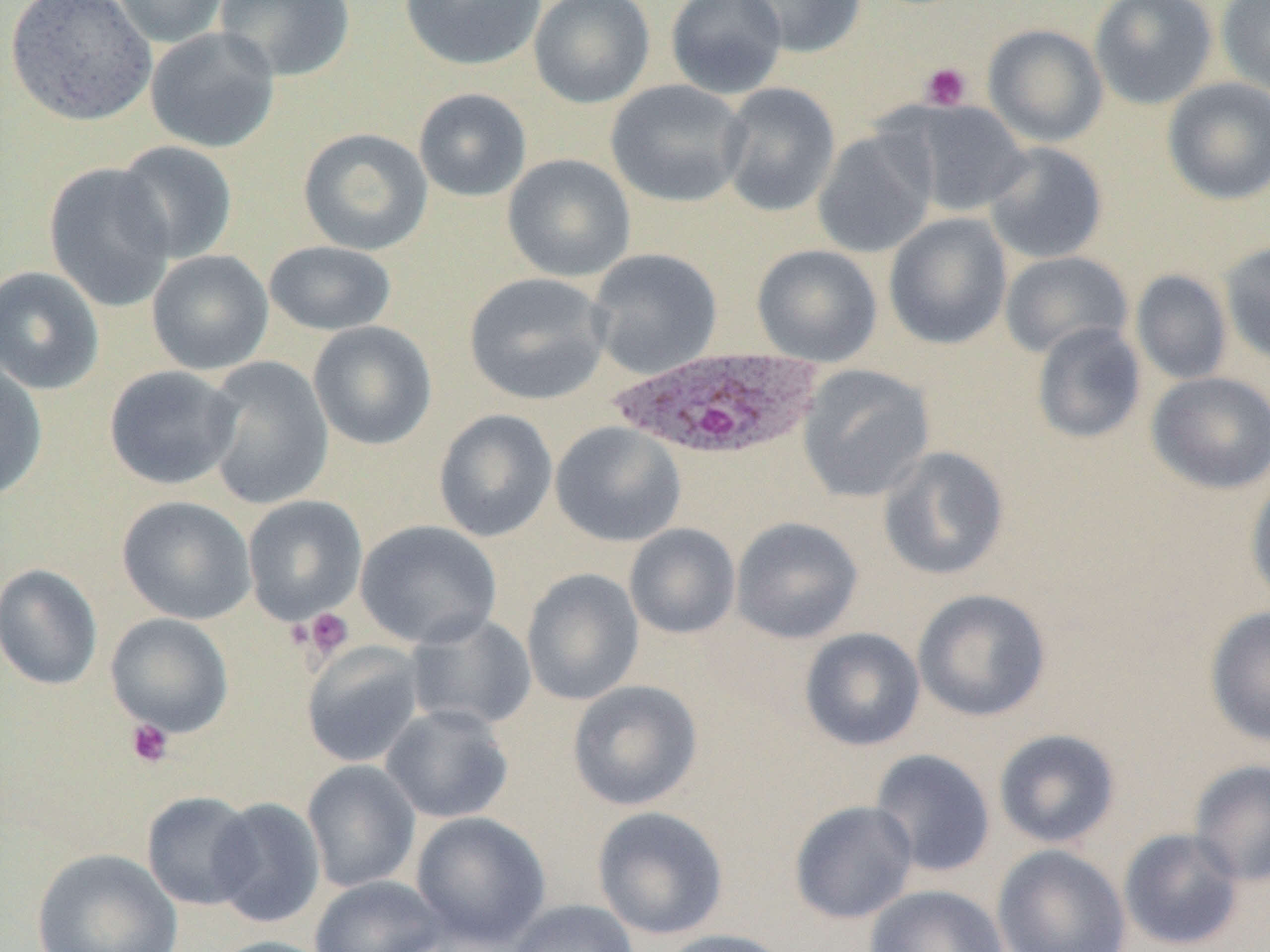
{
  "slide_level_diagnosis": "Plasmodium ovale",
  "uninfected_red_blood_cell_locations": "approximate bounding boxes as (x1, y1, x2, y2) in pixels: (3, 0, 157, 126), (109, 0, 230, 48), (213, 0, 355, 82), (399, 0, 547, 71), (529, 0, 655, 108), (665, 0, 788, 99), (733, 0, 867, 58), (1089, 0, 1218, 109), (1216, 0, 1270, 97), (983, 23, 1108, 147), (145, 26, 280, 153), (1162, 77, 1270, 205), (605, 79, 750, 208), (718, 82, 840, 217), (413, 88, 532, 202), (902, 101, 1032, 216), (298, 127, 433, 255), (813, 128, 937, 258), (113, 141, 238, 264), (983, 142, 1108, 264), (502, 153, 636, 282), (44, 162, 176, 312), (883, 213, 1013, 350), (1219, 240, 1270, 365), (264, 241, 397, 336), (751, 244, 883, 366), (586, 248, 722, 379), (146, 249, 274, 375), (999, 251, 1133, 360), (0, 265, 105, 395), (1131, 270, 1232, 385), (464, 272, 611, 406), (308, 321, 437, 450), (1031, 322, 1146, 444), (202, 356, 333, 510), (0, 358, 48, 501), (797, 364, 934, 503), (104, 365, 242, 490), (1146, 371, 1270, 494), (433, 409, 557, 542), (550, 421, 687, 547), (877, 445, 1009, 581), (1246, 476, 1270, 607), (116, 495, 256, 624), (242, 495, 367, 625), (730, 516, 863, 644), (355, 520, 501, 649), (624, 524, 741, 639), (0, 563, 103, 690), (521, 568, 644, 706), (912, 588, 1051, 722), (1205, 605, 1270, 747), (105, 612, 234, 736), (405, 613, 537, 731), (799, 627, 925, 751), (301, 641, 426, 768), (567, 679, 703, 811), (380, 704, 514, 824), (993, 729, 1121, 849), (868, 748, 996, 878), (1188, 758, 1270, 886), (302, 760, 421, 893), (141, 791, 260, 910), (209, 797, 326, 928), (789, 800, 918, 924), (592, 805, 729, 940), (411, 811, 551, 949), (1118, 828, 1245, 950), (992, 844, 1132, 952), (30, 847, 182, 952), (309, 874, 447, 951), (865, 884, 1010, 952), (506, 898, 640, 952), (655, 928, 794, 952), (205, 936, 340, 952)",
  "preparation": "thin blood film",
  "modality": "light microscopy",
  "plasmodium_ovale_infected_red_blood_cell_locations": "approximate bounding boxes as (x1, y1, x2, y2) in pixels: (609, 345, 827, 461)",
  "platelet_locations": "approximate bounding boxes as (x1, y1, x2, y2) in pixels: (920, 62, 972, 110), (300, 608, 354, 661), (126, 718, 174, 769)",
  "image_size": "1270×952 pixels",
  "field_of_view": "single",
  "magnification": "1000x"
}